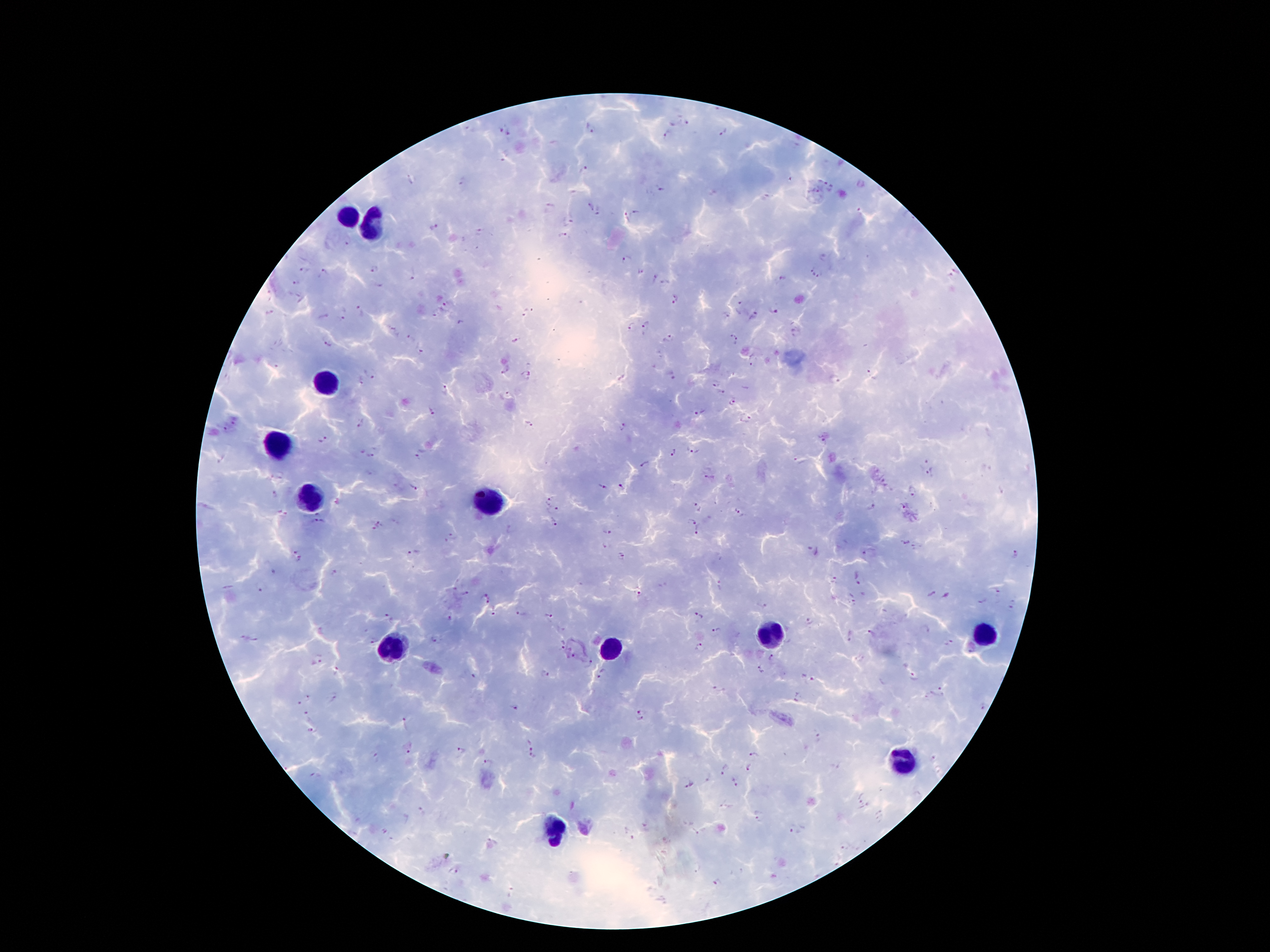
Approximate centers as {x, y} in pixels. Leukocyte locations: {347, 218}, {372, 222}, {323, 385}, {279, 446}, {307, 498}, {487, 503}, {775, 636}, {986, 636}, {393, 647}, {613, 648}, {900, 758}, {553, 831}. Plasmodium parasite locations: {686, 122}, {588, 129}, {500, 131}, {723, 133}, {509, 134}, {666, 135}, {585, 170}, {460, 181}, {661, 189}, {591, 206}, {552, 207}, {637, 211}, {597, 212}, {624, 217}, {569, 221}, {434, 227}, {479, 232}, {564, 235}, {345, 243}, {625, 260}, {372, 268}, {301, 270}, {954, 271}, {323, 273}, {812, 273}, {411, 277}, {822, 277}, {782, 279}, {654, 280}, {294, 283}, {379, 286}, {676, 300}, {740, 304}, {445, 307}, {363, 310}, {773, 311}, {270, 312}, {345, 313}, {755, 315}, {324, 316}, {724, 316}, {461, 322}, {631, 326}, {392, 328}, {646, 328}, {796, 331}, {409, 337}, {516, 339}, {670, 339}, {733, 339}, {329, 344}, {421, 352}, {751, 364}, {506, 370}, {371, 371}, {672, 375}, {528, 376}, {873, 376}, {836, 380}, {359, 381}, {716, 383}, {443, 389}, {723, 393}, {507, 394}, {733, 402}, {432, 412}, {700, 413}, {746, 421}, {233, 422}, {361, 424}, {530, 424}, {226, 428}, {623, 428}, {322, 439}, {823, 441}, {692, 450}, {361, 451}, {672, 452}, {373, 455}, {419, 458}, {924, 461}, {800, 463}, {646, 464}, {931, 472}, {709, 477}, {281, 478}, {602, 486}, {413, 487}, {622, 487}, {913, 491}, {275, 494}, {549, 501}, {699, 506}, {902, 506}, {871, 507}, {554, 510}, {740, 511}, {284, 513}, {320, 523}, {691, 523}, {378, 524}, {553, 524}, {607, 531}, {697, 532}, {451, 537}, {907, 543}, {604, 547}, {812, 552}, {865, 552}, {414, 553}, {622, 555}, {1016, 555}, {296, 557}, {273, 570}, {335, 571}, {859, 578}, {835, 580}, {261, 588}, {998, 592}, {465, 593}, {635, 593}, {931, 594}, {946, 595}, {486, 598}, {853, 598}, {982, 600}, {762, 606}, {1013, 606}, {520, 614}, {494, 615}, {387, 616}, {698, 616}, {549, 617}, {448, 619}, {809, 622}, {924, 630}, {716, 631}, {871, 633}, {242, 636}, {850, 636}, {254, 639}, {434, 639}, {372, 641}, {948, 642}, {561, 644}, {700, 647}, {573, 655}, {317, 659}, {773, 659}, {590, 664}, {337, 670}, {759, 670}, {545, 673}, {601, 673}, {474, 676}, {807, 676}, {913, 677}, {719, 691}, {937, 692}, {308, 696}, {335, 697}, {795, 697}, {299, 704}, {981, 706}, {516, 708}, {641, 710}, {305, 712}, {640, 720}, {405, 723}, {313, 730}, {818, 738}, {534, 744}, {407, 748}, {462, 752}, {754, 753}, {533, 757}, {374, 758}, {935, 758}, {488, 762}, {750, 766}, {726, 770}, {315, 775}, {709, 779}, {736, 781}, {689, 785}, {859, 799}, {725, 805}, {422, 812}, {758, 816}, {647, 826}, {695, 831}, {796, 831}, {629, 833}, {846, 847}, {454, 872}, {719, 883}. Thick blood film. Giemsa-stained preparation. One field from this slide. 100x magnification. Image is 1270×952 pixels. Patient malaria status: positive for Plasmodium falciparum. Photographed through the microscope eyepiece with a smartphone camera.